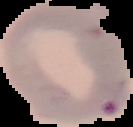
image size = 133×127 pixels
image type = segmented cell region on a black background
preparation = thin blood film
malaria status = parasitized